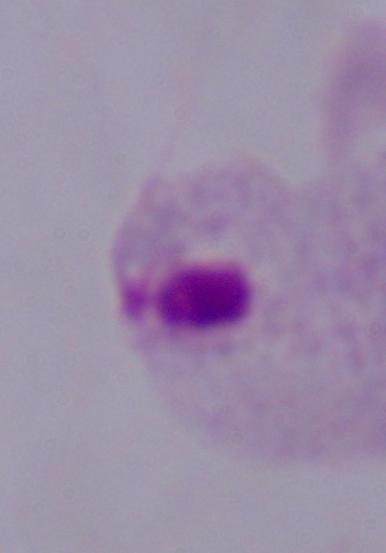
A trichomonad is seen. Micrograph. Captured at 1000x magnification.